Name the parasite shown.
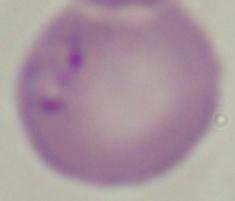

This is Babesia.

{
  "modality": "micrograph",
  "magnification": "1000x"
}